Describe the morphology of the red blood cells.
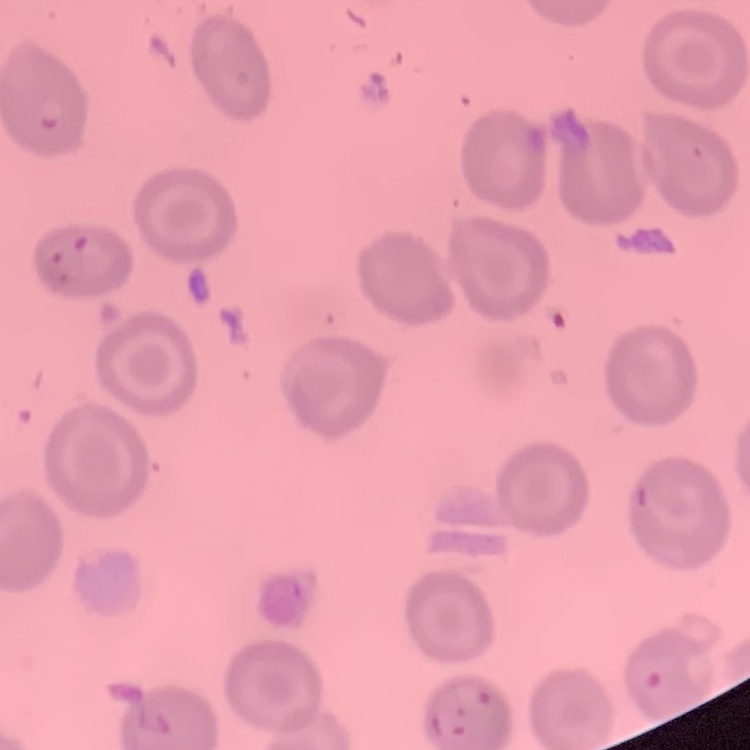
No rouleaux formation.

Thin blood smear. Square crop of a larger photomicrograph. Field's or Giemsa stain.